Locate every leukocyte (white blood cell).
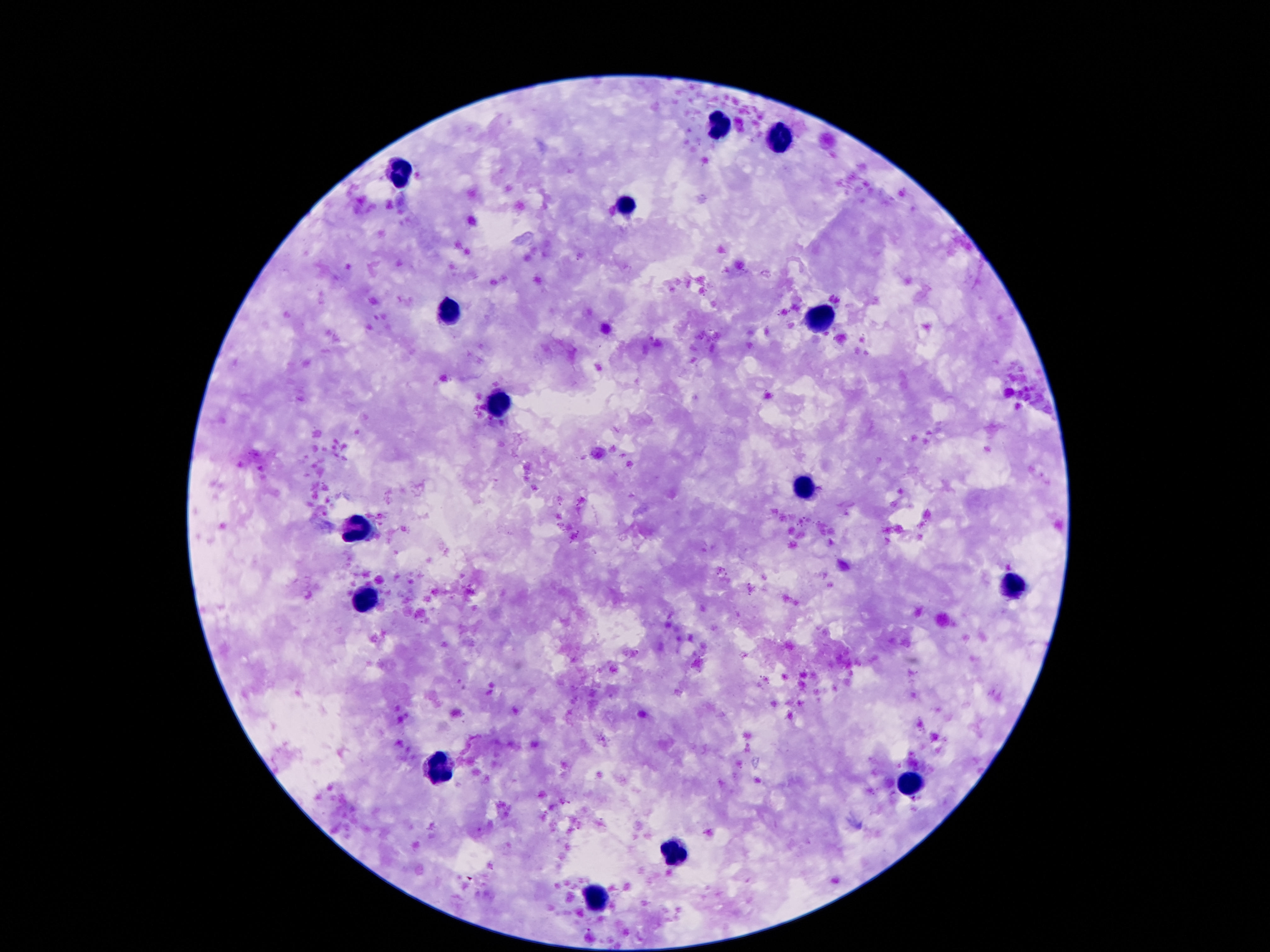

Approximate centers as {x, y} in pixels.
Leukocytes: {720, 128}, {776, 137}, {399, 173}, {625, 204}, {448, 309}, {821, 318}, {502, 400}, {802, 493}, {353, 526}, {1015, 589}, {366, 600}, {438, 770}, {910, 786}, {675, 857}, {595, 900}.

{
  "stain": "Giemsa",
  "image_size": "1270×952 pixels",
  "preparation": "thick blood smear",
  "capture": "smartphone camera through the microscope eyepiece",
  "field_of_view": "one from this slide",
  "magnification": "100x",
  "patient_malaria_status": "uninfected"
}